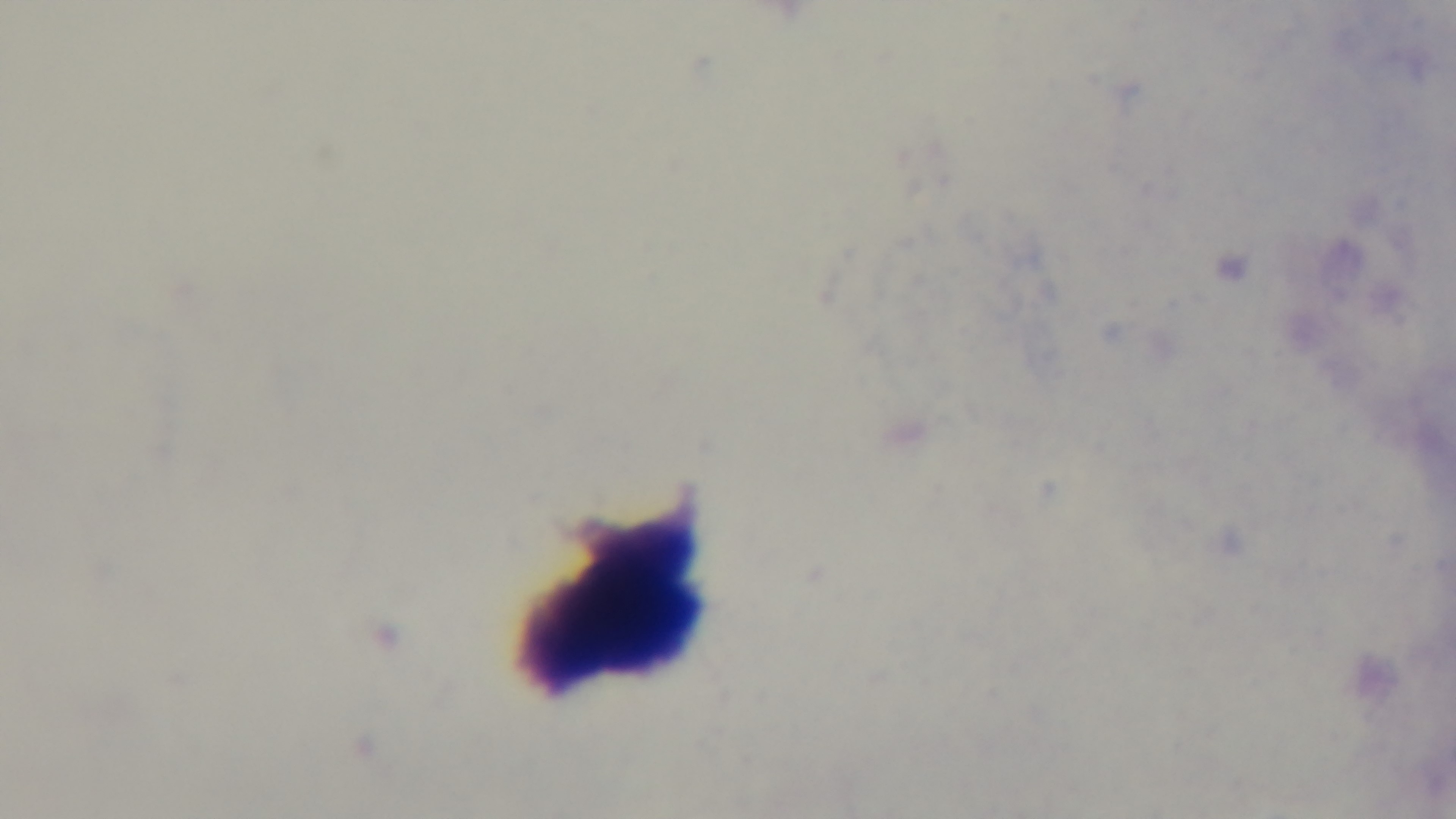 Light microscopy. 100x oil-immersion objective. Preparation: thick blood film. Captured with a mounted 4K digital camera. Malaria status: negative. Giemsa stain. Single field of view.